Describe the morphology of the red blood cells.
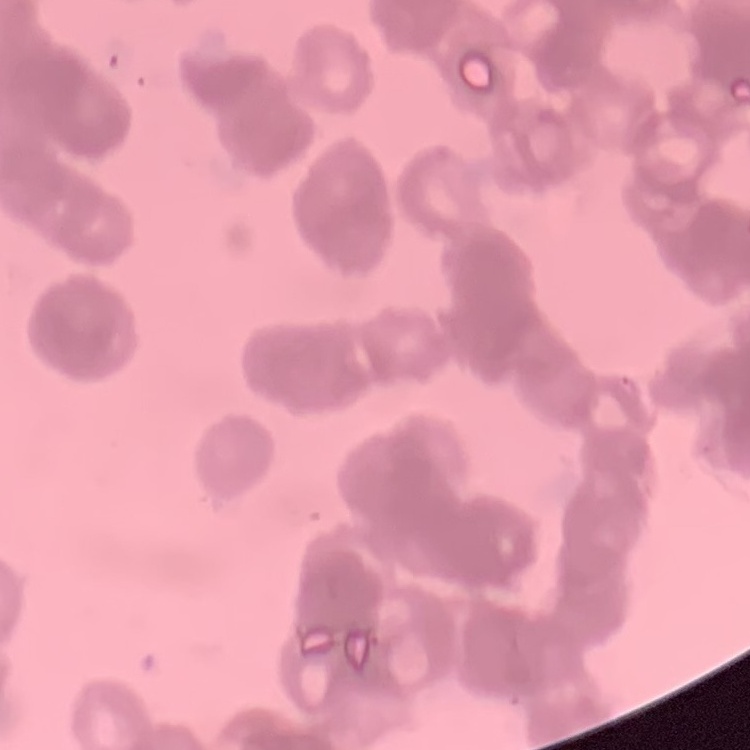

Rouleaux formation.

stain = Field's or Giemsa
preparation = thin peripheral smear
image type = square crop of a larger photomicrograph